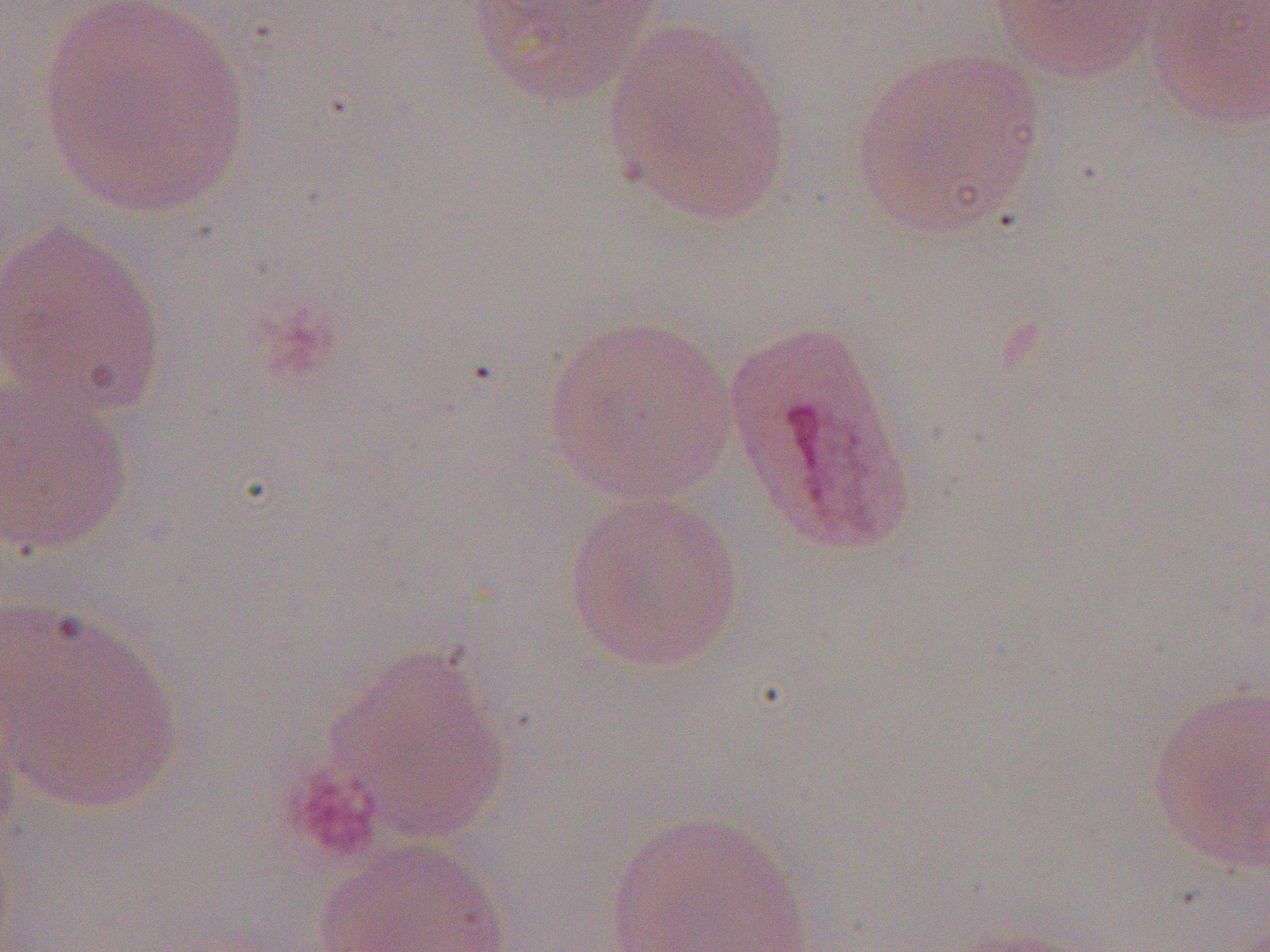

Summary:
  - Coordinate format: approximate bounding boxes as [x1, y1, x2, y2] in pixels
  - Uninfected red blood cell locations: [37, 0, 254, 217], [988, 0, 1163, 84], [1149, 0, 1270, 133], [465, 1, 664, 106], [602, 25, 792, 224], [848, 44, 1049, 239], [0, 221, 169, 417], [541, 314, 739, 502], [721, 317, 918, 557], [0, 369, 135, 557], [562, 489, 747, 672], [2, 597, 185, 814], [319, 643, 513, 845], [1144, 685, 1270, 875], [602, 809, 815, 951], [312, 838, 516, 952]
  - Slide-level diagnosis: Plasmodium ovale
  - Modality: light microscopy
  - Magnification: 1000x
  - Preparation: thin blood film
  - Field of view: one of a larger specimen
  - Image size: 1270×952 pixels